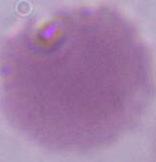
Summary:
  - Identification: red blood cell
  - Magnification: 1000x
  - Modality: micrograph